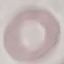

Summary:
  - Result: negative for malaria parasites
  - Preparation: thin smear
  - Capture: smartphone through the microscope eyepiece
  - Image type: cell patch, automatically extracted from a larger field of view and resized to 64 × 64 pixels
  - Stain: Giemsa